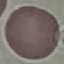

{
  "result": "no malaria parasites detected",
  "image_type": "automatically extracted cell patch, resized to 64 × 64 pixels",
  "capture": "smartphone camera at the microscope eyepiece",
  "preparation": "thin smear",
  "stain": "Giemsa"
}